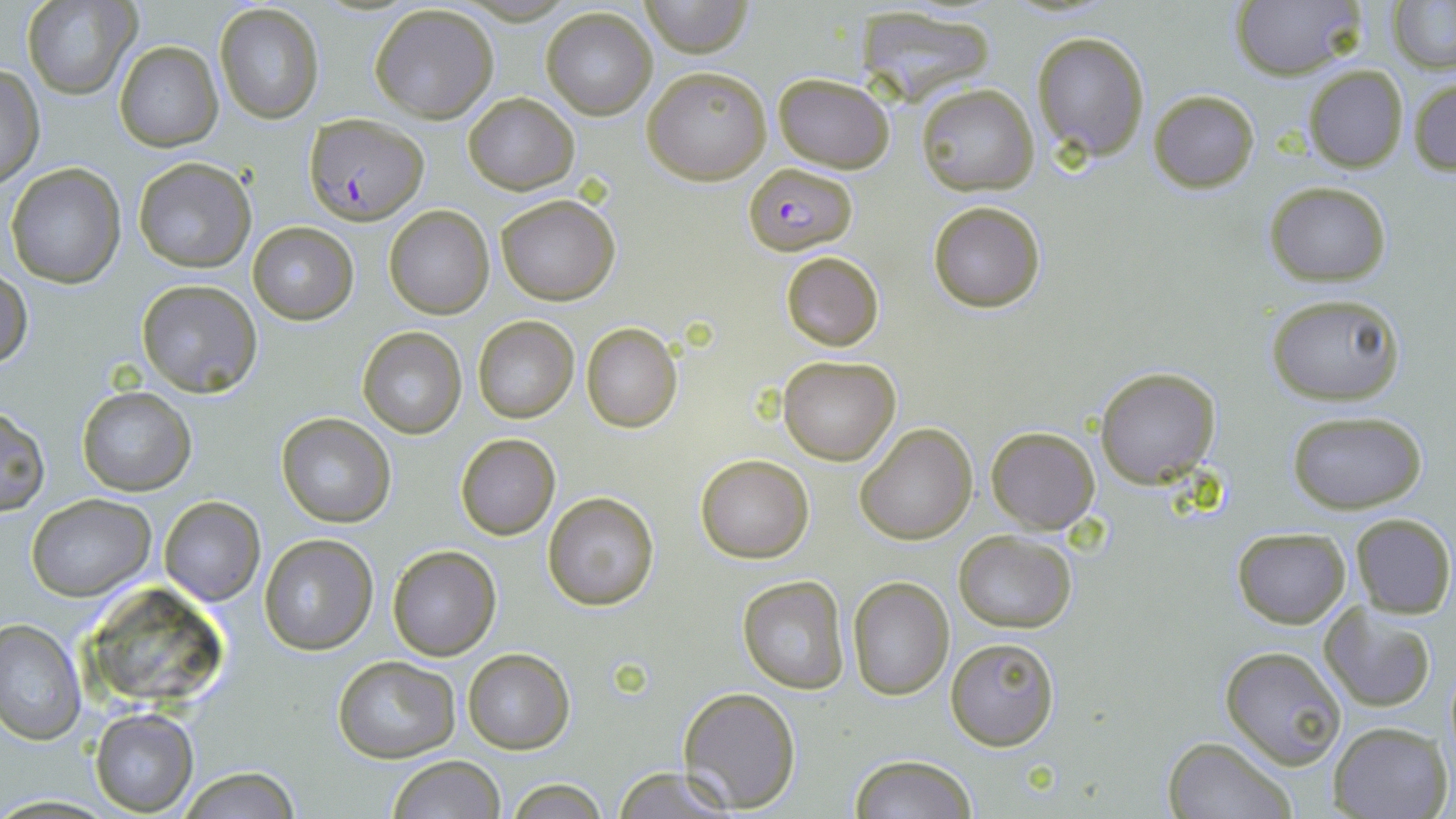

Summary:
  - Coordinate format: approximate bounding boxes as (x1, y1, x2, y2) in pixels
  - Plasmodium falciparum-infected red blood cell locations: (303, 112, 429, 226), (743, 163, 858, 256)
  - Uninfected red blood cell locations: (639, 0, 756, 57), (21, 1, 140, 99), (1229, 1, 1365, 81), (1387, 3, 1455, 73), (215, 4, 323, 123), (369, 5, 499, 124), (541, 7, 657, 120), (858, 7, 1000, 108), (1031, 29, 1149, 161), (114, 40, 223, 152), (1302, 65, 1408, 172), (1, 66, 44, 188), (643, 66, 770, 185), (772, 73, 895, 174), (1409, 75, 1456, 176), (917, 83, 1039, 195), (1148, 89, 1260, 191), (464, 92, 577, 194), (134, 158, 255, 271), (4, 163, 125, 288), (1265, 180, 1392, 286), (494, 193, 620, 305), (928, 201, 1044, 313), (384, 204, 494, 318), (247, 221, 358, 324), (780, 250, 885, 353), (1, 269, 32, 373), (135, 279, 263, 397), (1264, 291, 1406, 407), (472, 317, 579, 423), (581, 322, 683, 432), (355, 325, 467, 439), (777, 355, 899, 464), (1093, 365, 1221, 488), (77, 385, 195, 495), (1, 406, 49, 517), (1285, 410, 1430, 512), (276, 412, 395, 527), (856, 423, 978, 546), (986, 426, 1100, 533), (454, 432, 561, 541), (695, 453, 814, 563), (542, 492, 660, 611), (28, 494, 154, 601), (160, 498, 263, 605), (1349, 512, 1455, 618), (1232, 527, 1350, 627), (952, 529, 1077, 633), (259, 534, 379, 656), (386, 544, 502, 661), (738, 575, 849, 693), (848, 576, 953, 699), (92, 588, 228, 700), (1319, 604, 1438, 713), (0, 616, 85, 746), (946, 637, 1061, 751), (1220, 644, 1348, 769), (462, 648, 575, 754), (332, 654, 461, 765), (678, 687, 800, 812), (89, 707, 198, 814), (1326, 720, 1449, 819), (1161, 735, 1295, 818), (849, 754, 977, 819), (385, 755, 507, 819), (611, 765, 739, 819), (173, 767, 302, 819), (503, 779, 610, 817)
  - Slide-level diagnosis: Plasmodium falciparum
  - Magnification: 1000x
  - Stain: May-Grünwald-Giemsa
  - Preparation: thin blood film
  - Image size: 1456×819 pixels
  - Field of view: one of a larger specimen
  - Modality: light microscopy